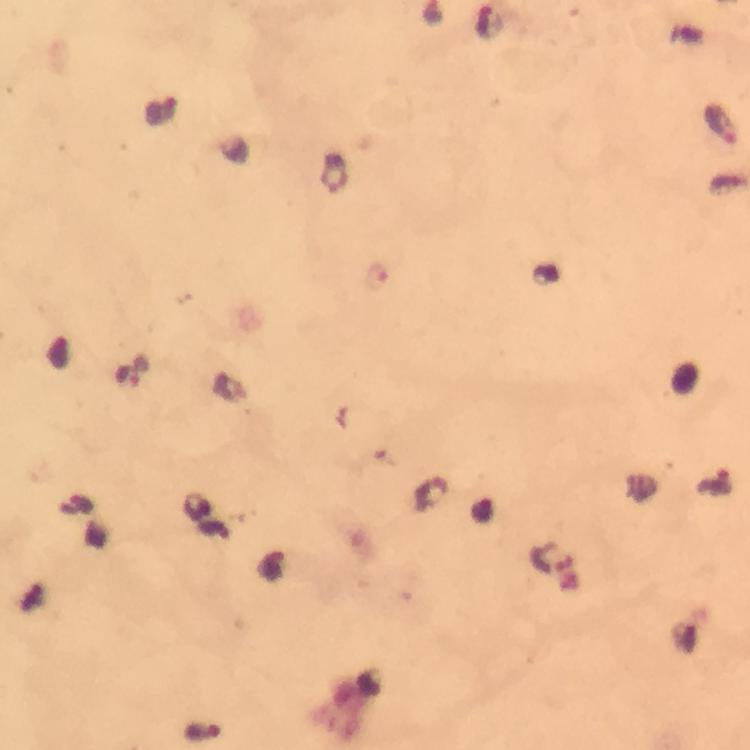
cropped from = one field of view
magnification = 100x
image size = 750×750 pixels
preparation = thick blood smear
capture = smartphone photograph through a microscope
immersion oil = used
malaria parasite locations = approximate centers as [x, y] in pixels: [488, 22], [161, 107], [722, 123], [378, 276], [129, 376], [717, 482], [544, 558], [203, 733]
context = from a diagnostic examination for malaria
stain = Giemsa